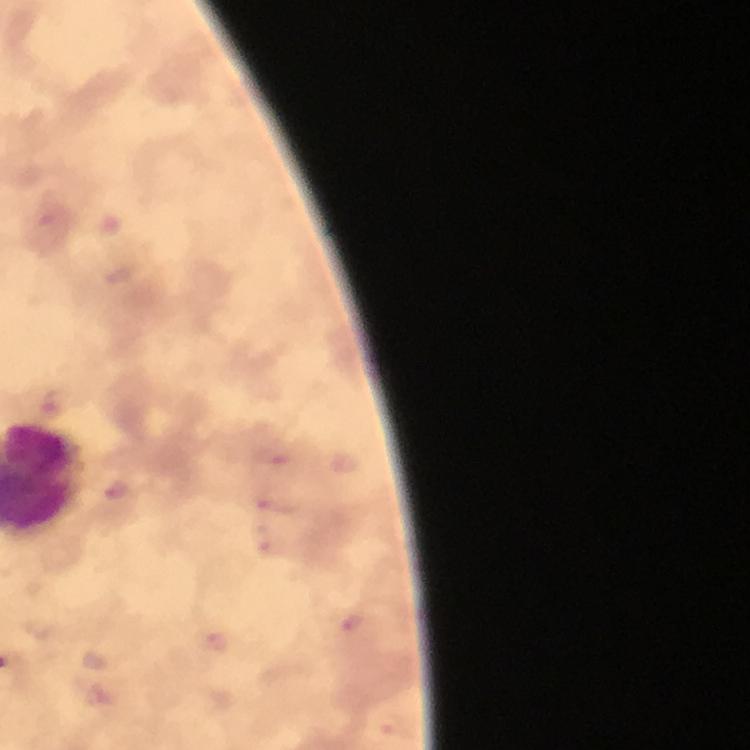

Approximate centers as (x, y) in pixels. Plasmodium parasite locations: (277, 457), (115, 488), (275, 505), (353, 621). Giemsa-stained preparation. Image is 750×750 pixels. Photographed with a smartphone mounted on the microscope. Cropped region of a single field of view. From a diagnostic examination for malaria. Immersion oil was used. 100x magnification. Thick blood film.